Describe the morphology of the erythrocytes.
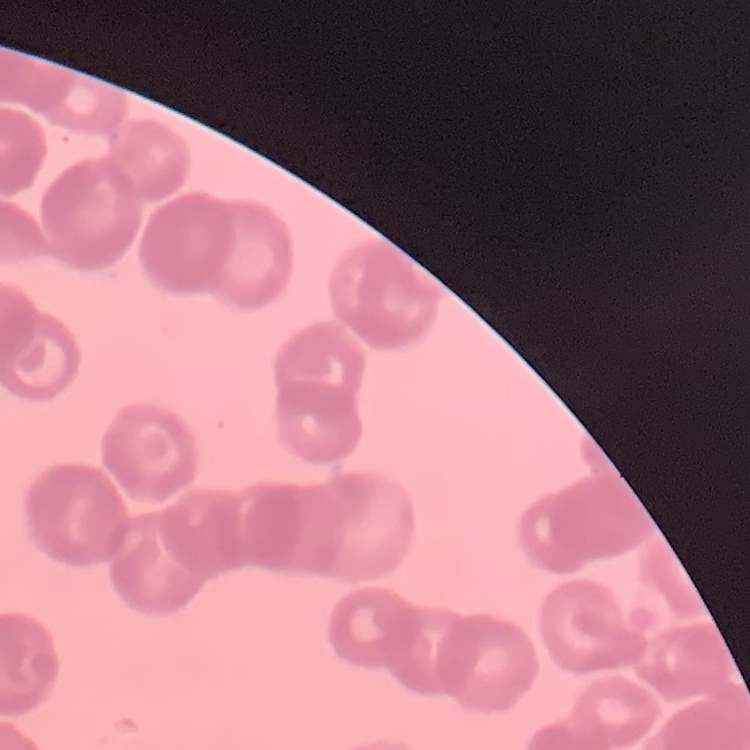
They show rouleaux formation.

image_type: square crop of a larger photomicrograph
preparation: thin blood film
stain: Field's or Giemsa